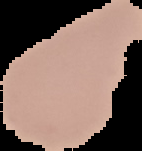

result = negative for malaria parasites
image size = 142×151 pixels
image type = segmented cell region on a black background
preparation = thin blood smear